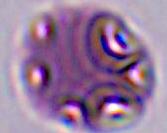

identification = Plasmodium
magnification = 400x or 1000x
modality = micrograph